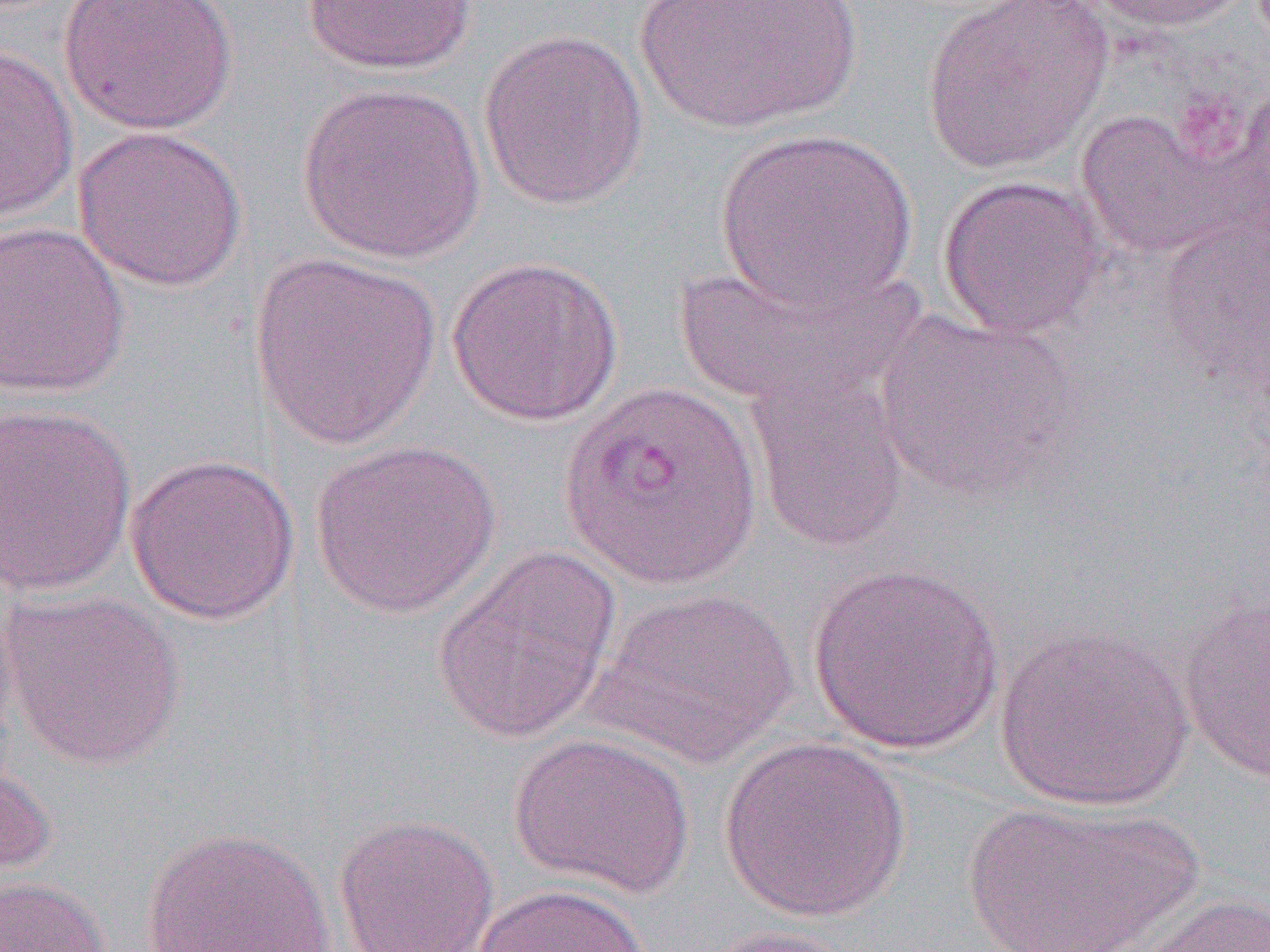
slide-level diagnosis = Plasmodium vivax
image size = 1270×952 pixels
modality = light microscopy
preparation = thin blood smear
uninfected red blood cell locations = approximate bounding boxes as (x1,y1)-(x2,y2) corner pairs in pixels: (58,0)-(239,135), (301,0)-(479,75), (920,0)-(1115,174), (1082,0)-(1255,32), (632,1)-(861,134), (478,28)-(650,211), (0,43)-(78,223), (296,80)-(486,264), (1077,107)-(1249,262), (73,126)-(248,292), (714,127)-(918,316), (937,174)-(1107,341), (0,220)-(131,399), (246,251)-(441,452), (446,255)-(625,427), (669,263)-(921,412), (873,308)-(1082,503), (744,364)-(909,554), (1,401)-(137,598), (308,438)-(501,619), (125,451)-(299,625), (431,543)-(623,743), (807,562)-(1006,755), (1,588)-(185,770), (589,588)-(799,767), (1177,589)-(1270,785), (994,625)-(1195,812), (507,731)-(695,900), (717,736)-(912,923), (0,752)-(56,882), (955,797)-(1205,952), (333,813)-(500,952), (139,825)-(339,952), (0,875)-(113,952), (471,882)-(652,952), (1108,890)-(1270,952), (688,925)-(863,951)
magnification = 1000x
Plasmodium vivax-infected red blood cell locations = approximate bounding boxes as (x1,y1)-(x2,y2) corner pairs in pixels: (558,378)-(764,593)
field of view = single